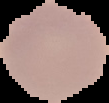
preparation = thin blood smear
image type = segmented cell region on a black background
malaria status = uninfected
image size = 109×103 pixels